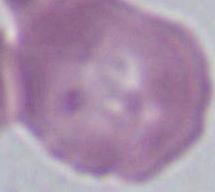
magnification: 1000x
modality: micrograph
identification: red blood cell